Give the preparation type.
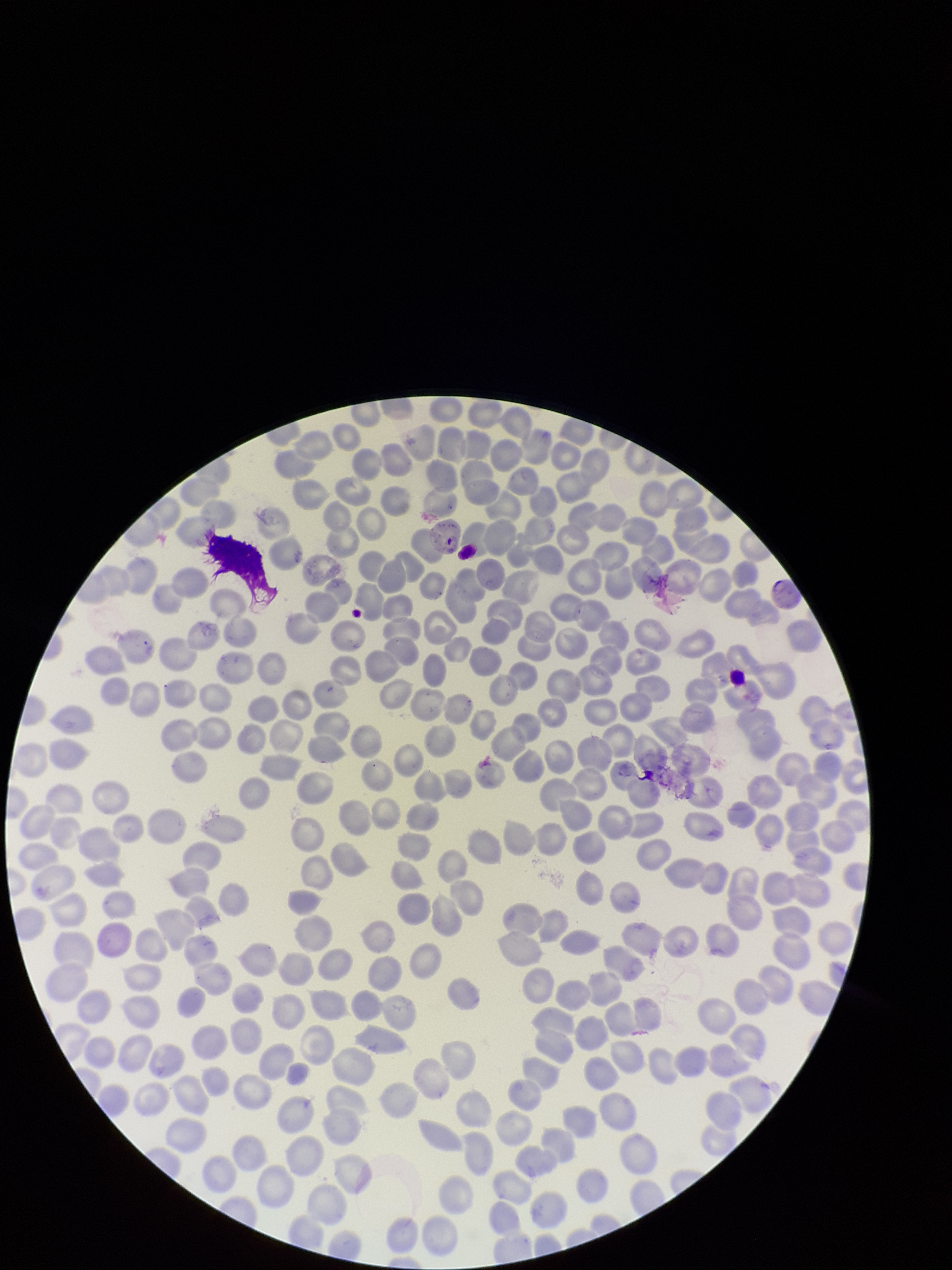
Thin.

Red blood cell count: 241. Species reported for this patient: Plasmodium falciparum. Single field of view. Parasitized red blood cells: identified. Photographed through the microscope eyepiece with a smartphone camera. Patient malaria status: positive. Parasitized red blood cell count: 3. Image is 952×1270 pixels. Giemsa stain.